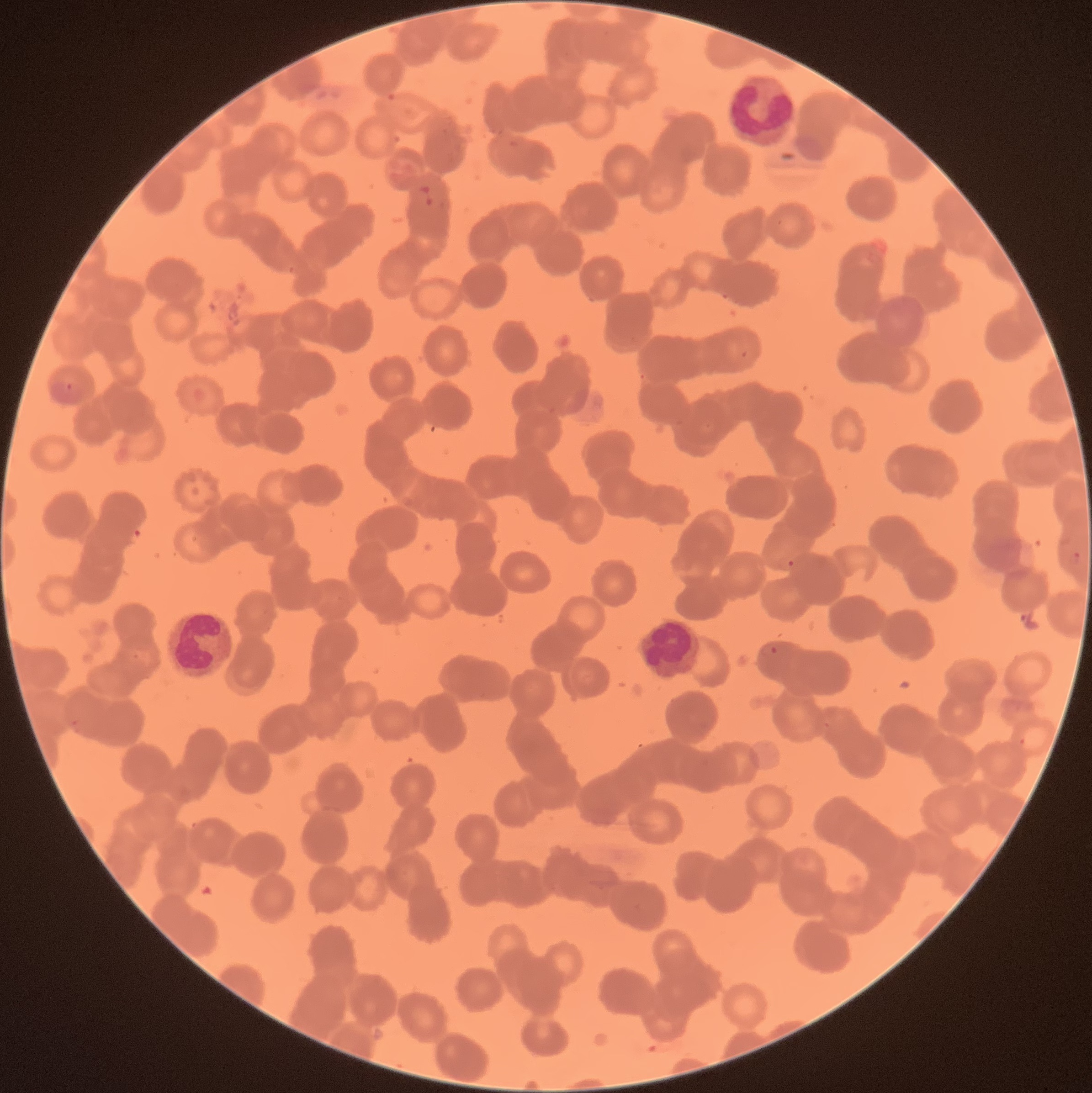
coordinate format = approximate bounding boxes as (x1,y1)-(x2,y2) corner pairs in pixels
Plasmodium parasites too small for a box (approximate centers as (x,y) in pixels) = (70,386)
Plasmodium parasite locations = (1069,550)-(1082,566), (775,556)-(794,572), (758,642)-(780,657)
white blood cell locations = (725,74)-(797,151), (171,612)-(233,680), (638,616)-(702,679)
red blood cell morphology = rouleaux formation
image size = 1092×1093 pixels
modality = light microscopy
preparation = thin blood smear